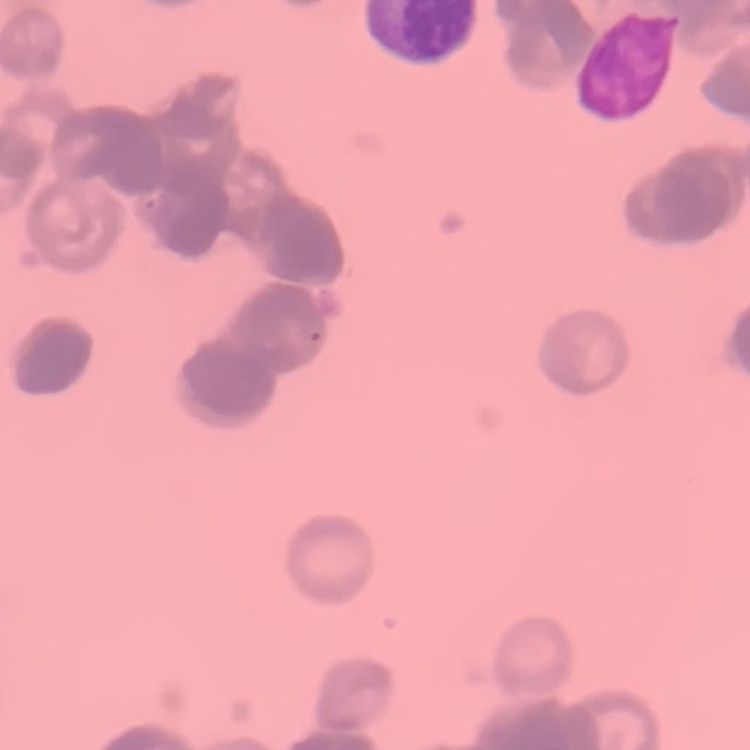 The erythrocytes exhibit rouleaux formation. Thin peripheral smear. Field's or Giemsa stain. Square crop of a larger photomicrograph.